Identify the parasite.
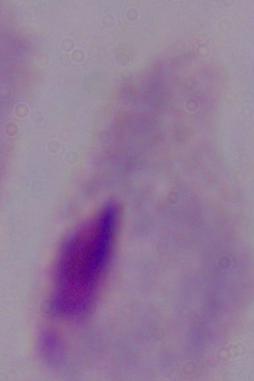

A trichomonad.

Summary:
  - Modality: photomicrograph
  - Magnification: 1000x